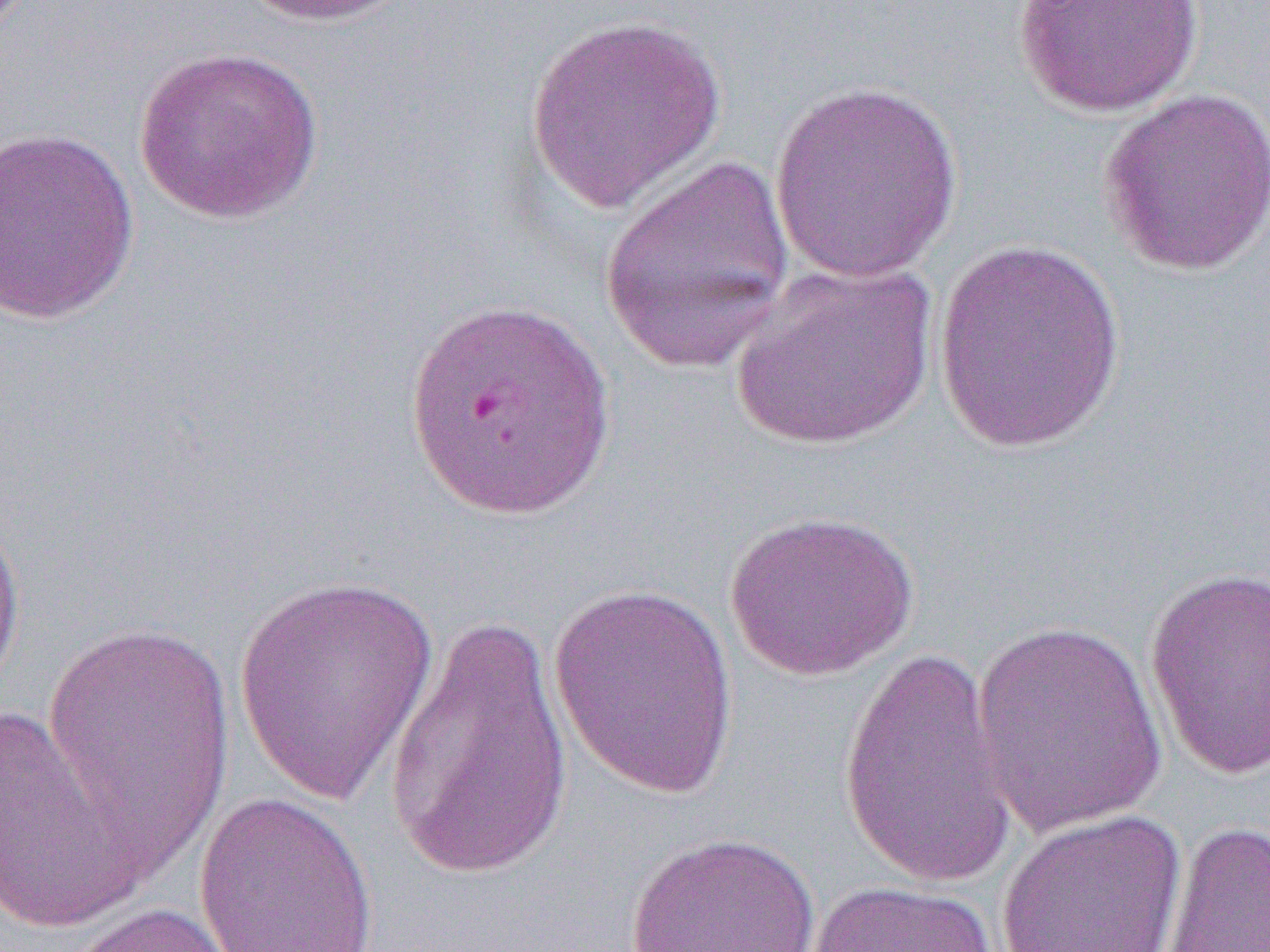
Summary:
  - Coordinate format: approximate bounding boxes as (x1,y1)-(x2,y2) corner pairs in pixels
  - Uninfected red blood cell locations: (240,0)-(417,28), (1013,1)-(1203,118), (524,13)-(725,213), (133,46)-(325,225), (768,80)-(965,284), (1098,87)-(1270,277), (0,128)-(140,326), (597,156)-(798,374), (934,240)-(1128,453), (729,261)-(939,451), (405,294)-(616,520), (0,498)-(27,705), (721,509)-(921,682), (1143,567)-(1270,781), (232,571)-(440,808), (547,580)-(742,797), (383,611)-(575,885), (39,617)-(239,875), (970,619)-(1168,838), (837,646)-(1018,894), (0,696)-(144,936), (193,790)-(380,952), (996,809)-(1186,952), (1160,820)-(1270,951), (623,831)-(823,952), (803,879)-(999,952), (51,899)-(259,952)
  - Slide-level diagnosis: Plasmodium falciparum
  - Preparation: thin blood film
  - Image size: 1270×952 pixels
  - Field of view: single
  - Modality: light microscopy
  - Magnification: 1000x